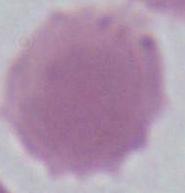
Summary:
  - Identification: red blood cell
  - Modality: photomicrograph
  - Magnification: 1000x